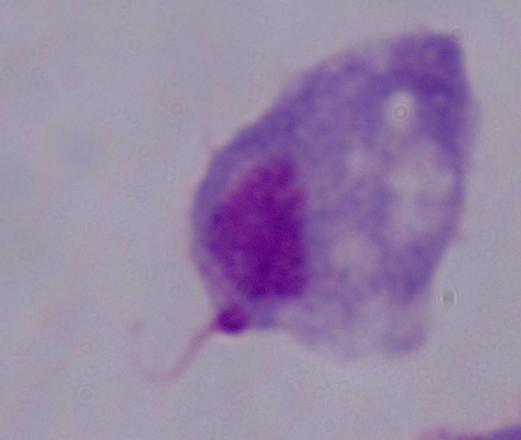

identification = trichomonad
modality = micrograph
magnification = 1000x